Locate every Plasmodium parasite.
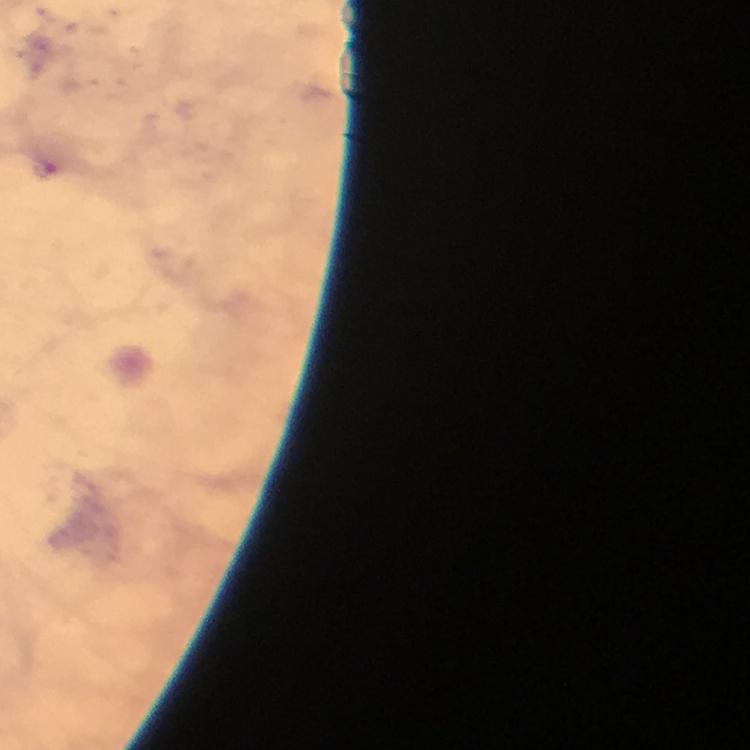
Approximate centers as (x, y) in pixels.
Plasmodium parasites: (46, 170).

capture = smartphone photograph through a microscope
cropped from = a single field of view
preparation = thick blood smear
immersion oil = used
context = from a diagnostic examination for malaria
stain = Giemsa
image size = 750×750 pixels
magnification = 100x